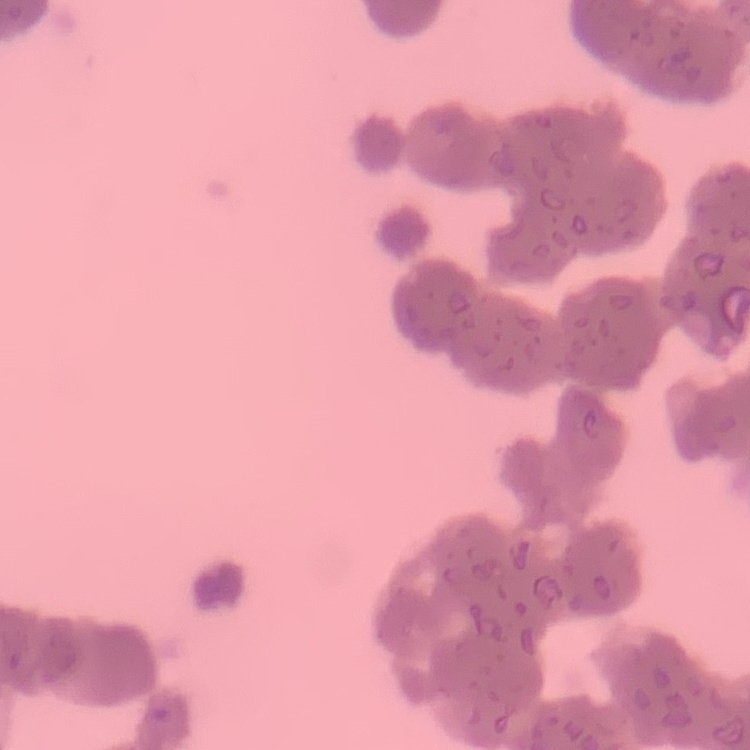 The erythrocytes show rouleaux formation. Thin blood smear. One tile cut from a larger photomicrograph. Stained with either Field's or Giemsa.